Assess this cell for malaria.
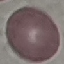
It is uninfected.

stain: Giemsa
image_type: automatically extracted cell patch, resized to 64 × 64 pixels
capture: smartphone camera at the microscope eyepiece
preparation: thin smear